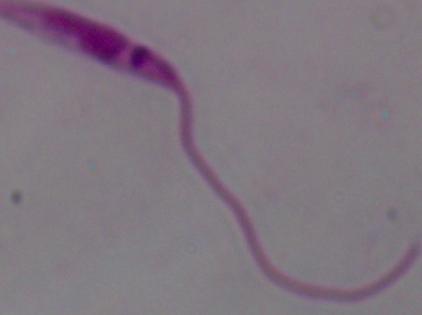
identification = Leishmania
modality = photomicrograph
magnification = 1000x